Give the extent of all Plasmodium vivax-infected red blood cells.
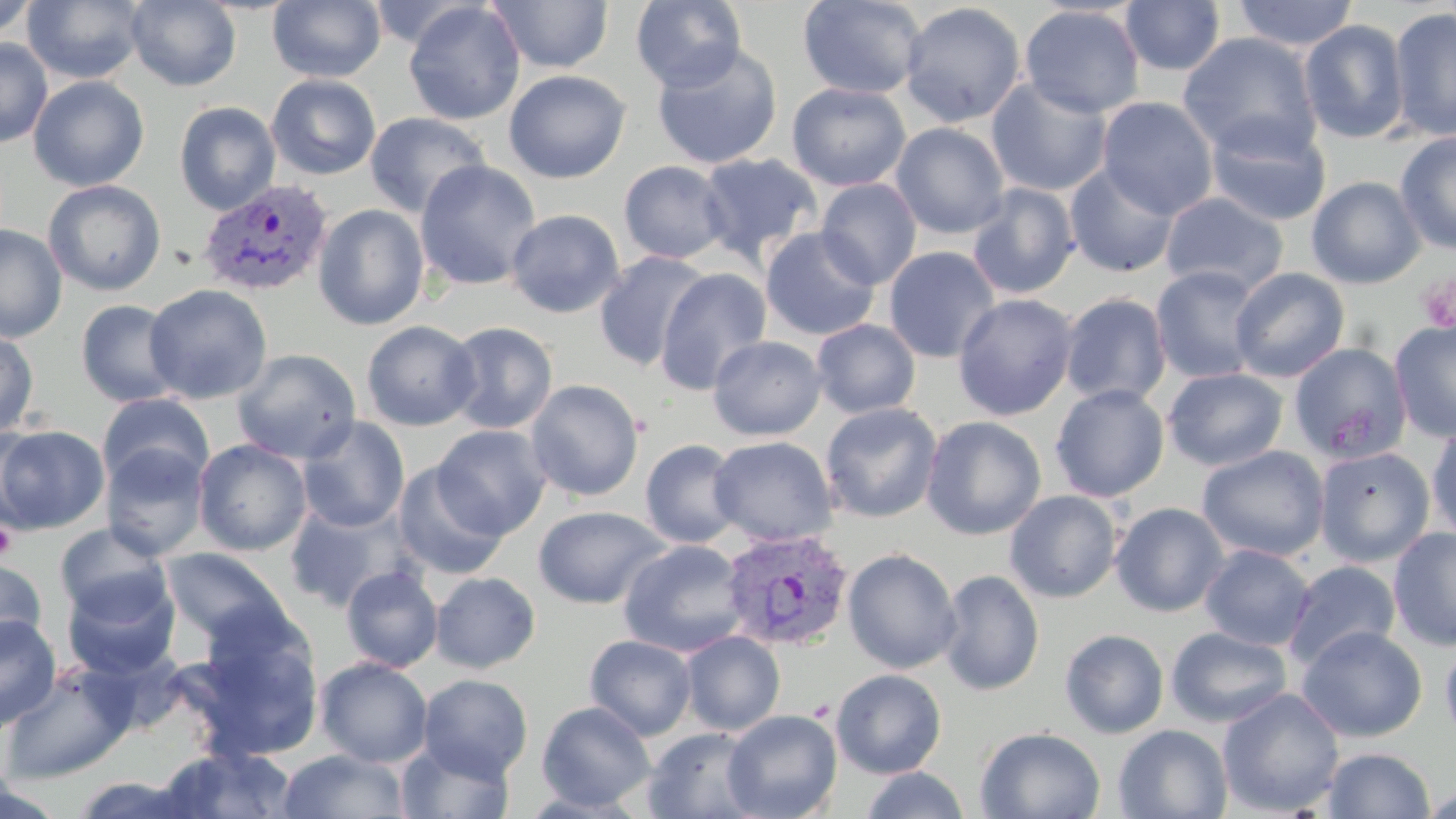

Approximate bounding boxes as (x1, y1, x2, y2) in pixels.
Plasmodium vivax-infected red blood cells: (197, 180, 335, 297), (719, 529, 853, 652).

slide-level diagnosis = Plasmodium vivax
stain = May-Grünwald-Giemsa
modality = optical microscopy
magnification = 1000x
image size = 1456×819 pixels
uninfected red blood cell locations = approximate bounding boxes as (x1, y1, x2, y2) in pixels: (0, 0, 39, 41), (21, 0, 148, 85), (126, 0, 241, 91), (268, 0, 386, 83), (485, 0, 615, 74), (631, 0, 747, 92), (797, 0, 926, 99), (1119, 0, 1226, 75), (1232, 0, 1359, 52), (404, 2, 525, 126), (900, 2, 1026, 127), (1019, 5, 1145, 118), (1388, 7, 1456, 143), (1298, 19, 1410, 144), (1179, 33, 1323, 160), (0, 38, 53, 147), (651, 42, 783, 170), (503, 69, 631, 184), (266, 74, 381, 180), (28, 76, 150, 191), (986, 76, 1113, 196), (787, 82, 911, 191), (1097, 96, 1219, 219), (174, 101, 281, 215), (364, 112, 491, 218), (1205, 115, 1332, 227), (890, 122, 1010, 239), (1396, 131, 1456, 255), (696, 153, 823, 266), (415, 160, 541, 291), (619, 160, 733, 264), (1064, 163, 1180, 278), (1306, 176, 1426, 289), (815, 178, 922, 289), (43, 179, 166, 296), (966, 183, 1080, 300), (1160, 192, 1289, 296), (313, 204, 430, 330), (505, 209, 625, 318), (0, 225, 67, 342), (760, 227, 881, 341), (883, 246, 1001, 363), (593, 251, 713, 372), (1150, 265, 1265, 384), (655, 267, 772, 395), (1229, 267, 1350, 381), (144, 284, 273, 405), (952, 293, 1079, 421), (1059, 293, 1172, 407), (75, 299, 184, 407), (811, 319, 921, 418), (1389, 319, 1456, 443), (361, 320, 481, 431), (443, 321, 558, 434), (0, 329, 40, 438), (707, 335, 827, 440), (1292, 341, 1410, 464), (232, 348, 362, 464), (1162, 367, 1288, 472), (526, 379, 645, 502), (1050, 384, 1170, 502), (97, 392, 214, 494), (820, 403, 942, 523), (921, 415, 1047, 540), (296, 416, 410, 532), (1426, 423, 1456, 546), (0, 424, 110, 535), (432, 425, 552, 539), (708, 436, 839, 547), (193, 439, 313, 556), (640, 439, 744, 548), (100, 442, 210, 560), (1197, 445, 1330, 562), (1313, 446, 1435, 567), (392, 462, 509, 580), (1004, 489, 1123, 603), (283, 498, 416, 613), (1110, 502, 1230, 617), (532, 505, 669, 609), (54, 522, 175, 626), (1388, 527, 1456, 652), (618, 539, 750, 657), (1199, 544, 1315, 651), (160, 547, 291, 649), (843, 548, 961, 673), (0, 557, 47, 659), (1283, 560, 1401, 671), (341, 565, 443, 673), (937, 569, 1045, 696), (430, 571, 540, 673), (61, 572, 179, 681), (0, 613, 61, 732), (187, 620, 326, 762), (1297, 625, 1428, 742), (1165, 626, 1292, 728), (1060, 628, 1169, 738), (680, 630, 786, 735), (585, 635, 697, 740), (1440, 635, 1456, 750), (315, 657, 433, 767), (0, 662, 137, 784), (831, 668, 947, 778), (418, 674, 533, 780), (1217, 687, 1345, 817), (536, 701, 655, 811), (722, 709, 842, 819), (1113, 724, 1232, 819), (642, 726, 764, 819), (975, 726, 1105, 819), (396, 739, 515, 819), (156, 745, 299, 818), (1322, 747, 1436, 818), (277, 749, 410, 818), (860, 767, 970, 819), (67, 773, 202, 817), (0, 782, 68, 819), (1420, 782, 1456, 819)
platelet locations = approximate bounding boxes as (x1, y1, x2, y2) in pixels: (1417, 273, 1456, 334), (0, 521, 17, 559)
field of view = single
preparation = thin blood smear